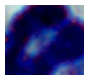
A leukocyte is seen. Captured at 1000x magnification. Micrograph.